Give the preparation type.
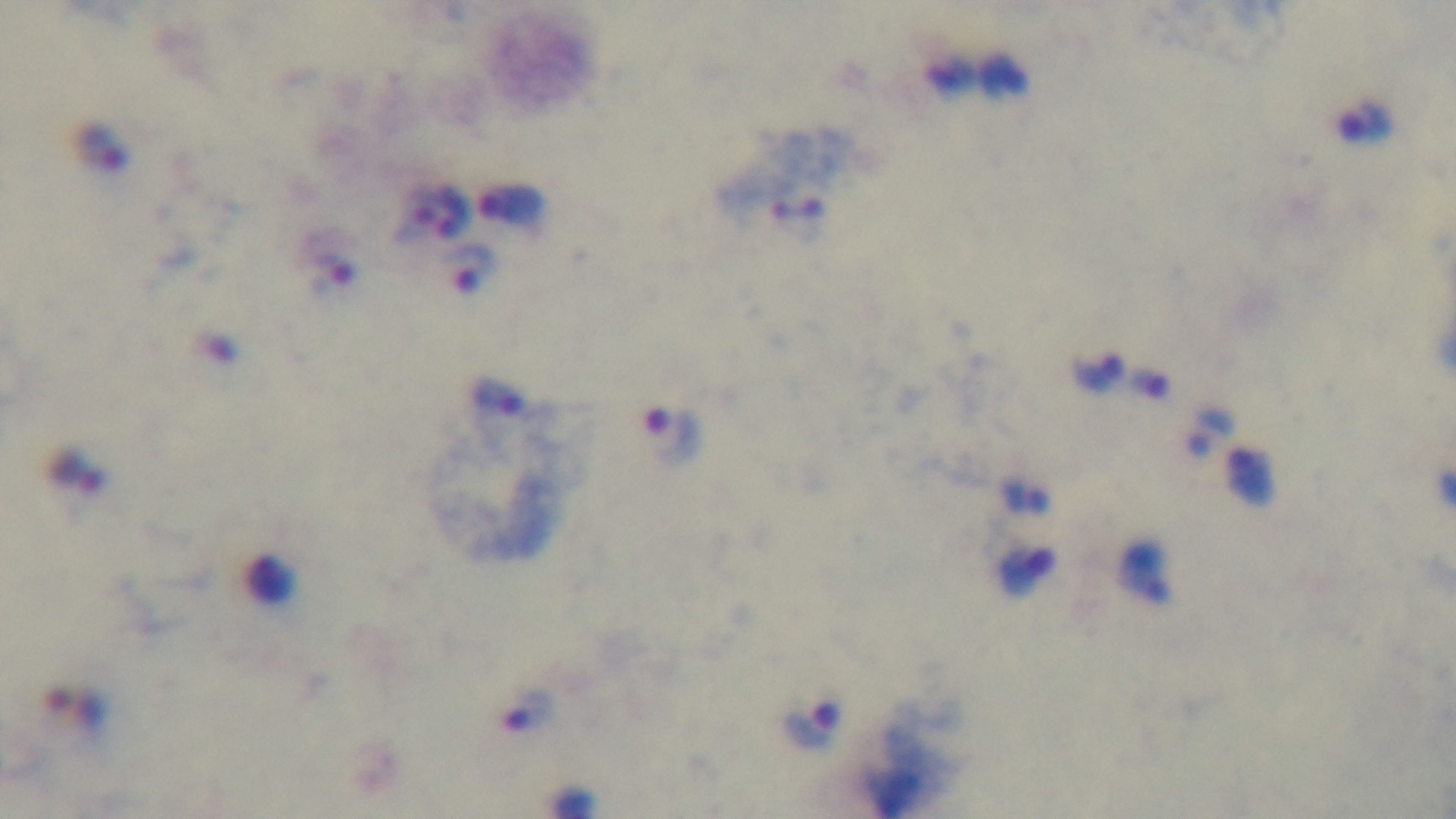

It is a thick blood film.

capture = mounted 4K digital camera
field of view = one from the slide
malaria status = positive
modality = light microscopy
stain = Giemsa
objective = 100x oil immersion